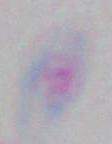

magnification = 1000x
identification = Toxoplasma gondii
modality = photomicrograph